Find each parasitized RBC.
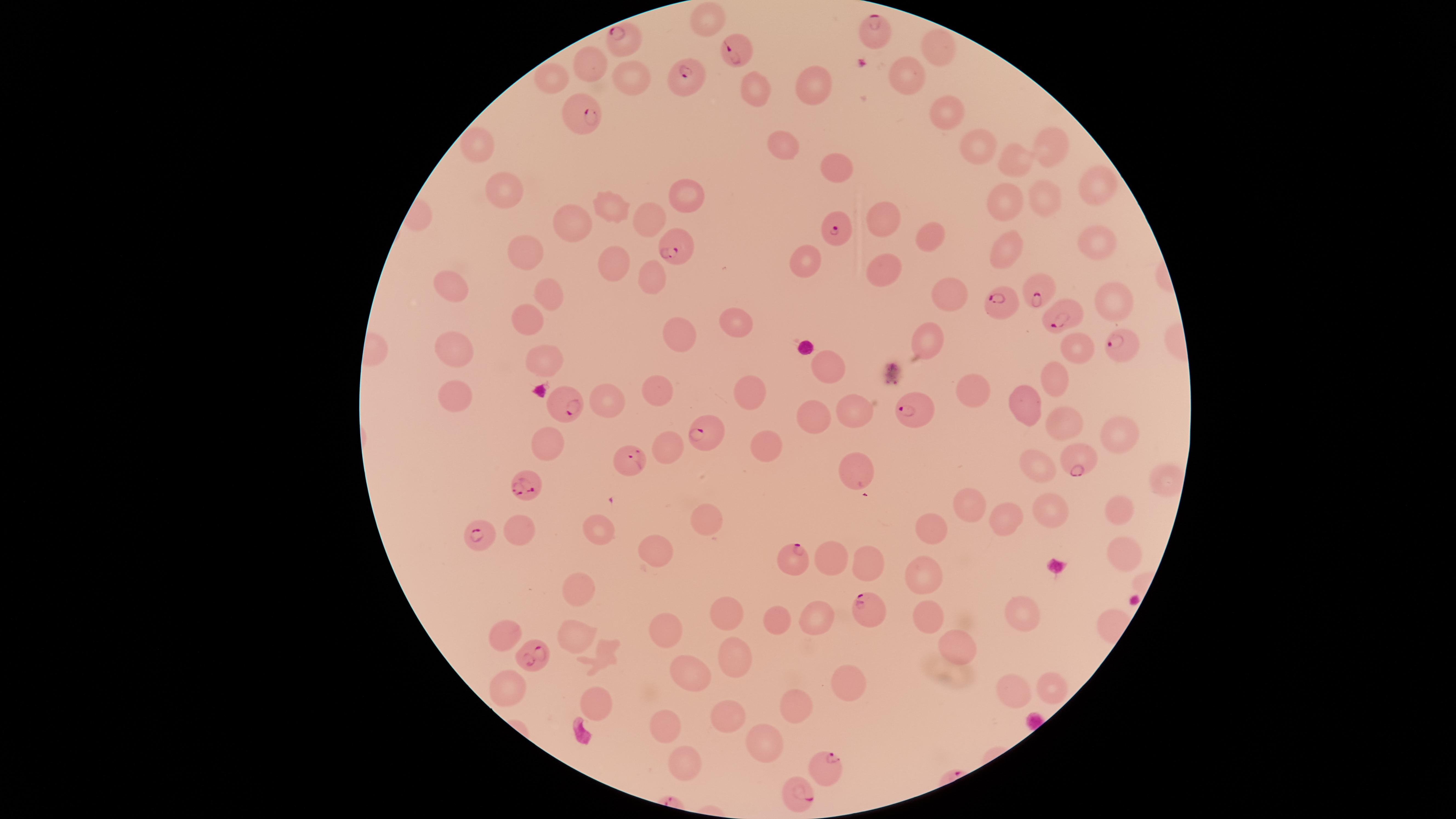

Approximate marker points, in pixels from the top-left corner.
Parasitized RBCs: (x=876, y=30), (x=631, y=37), (x=734, y=52), (x=685, y=78), (x=584, y=118), (x=839, y=229), (x=675, y=249), (x=1034, y=289), (x=1002, y=302), (x=1060, y=313), (x=1121, y=346), (x=567, y=402), (x=915, y=408), (x=706, y=437), (x=1075, y=459), (x=629, y=460), (x=526, y=487), (x=479, y=535), (x=789, y=557), (x=867, y=612), (x=539, y=657), (x=828, y=765), (x=800, y=792).

field of view = single
stain = Giemsa
capture = smartphone photograph through the microscope eyepiece
preparation = thin blood smear
visible region = circular
uninfected RBCs = approximate marker points, in pixels from the top-left corner: (x=708, y=18), (x=936, y=48), (x=592, y=63), (x=908, y=73), (x=634, y=79), (x=554, y=80), (x=814, y=82), (x=756, y=91), (x=951, y=110), (x=486, y=142), (x=785, y=142), (x=980, y=146), (x=1046, y=146), (x=1017, y=163), (x=835, y=166), (x=1094, y=184), (x=504, y=187), (x=692, y=196), (x=1046, y=197), (x=1006, y=202), (x=611, y=209), (x=651, y=214), (x=883, y=218), (x=578, y=219), (x=929, y=237), (x=1096, y=239), (x=527, y=249), (x=1005, y=251), (x=613, y=264), (x=805, y=264), (x=886, y=270), (x=656, y=271), (x=449, y=287), (x=554, y=292), (x=953, y=295), (x=1118, y=302), (x=529, y=319), (x=734, y=322), (x=678, y=335), (x=925, y=340), (x=455, y=343), (x=1080, y=344), (x=538, y=353), (x=818, y=363), (x=1053, y=373), (x=658, y=385), (x=973, y=388), (x=455, y=390), (x=747, y=392), (x=612, y=398), (x=1025, y=399), (x=853, y=409), (x=808, y=414), (x=1057, y=420), (x=1118, y=432), (x=545, y=437), (x=669, y=441), (x=1036, y=460), (x=856, y=475), (x=1165, y=482), (x=972, y=502), (x=1053, y=508), (x=1114, y=511), (x=1007, y=518), (x=707, y=520), (x=521, y=523), (x=934, y=527), (x=597, y=536), (x=654, y=546), (x=1123, y=550), (x=831, y=555), (x=866, y=563), (x=924, y=569), (x=581, y=593), (x=725, y=604), (x=1022, y=607), (x=779, y=612), (x=927, y=613), (x=815, y=620), (x=578, y=630), (x=667, y=630), (x=506, y=636), (x=962, y=643), (x=737, y=656), (x=610, y=657), (x=694, y=669), (x=849, y=683), (x=1047, y=686), (x=1008, y=691), (x=507, y=694), (x=596, y=704), (x=797, y=706), (x=731, y=715), (x=659, y=721), (x=768, y=740), (x=685, y=753)
species = Plasmodium falciparum
image size = 1456×819 pixels